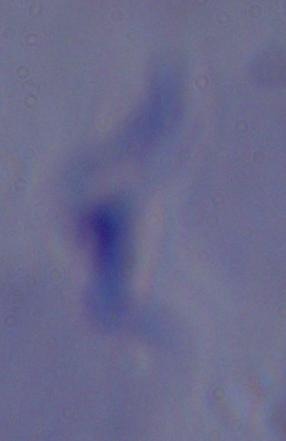

A trypanosome is shown. 1000x magnification. Micrograph.